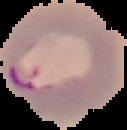
preparation: thin blood film
image_size: 127×130 pixels
image_type: cell region segmented out of the field of view; surrounding area masked to black
result: Plasmodium parasites detected